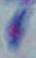

{
  "magnification": "1000x",
  "identification": "Toxoplasma gondii",
  "modality": "micrograph"
}